Assess this cell for malaria.
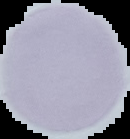
Uninfected.

Summary:
  - Image size: 130×139 pixels
  - Preparation: thin blood film
  - Image type: cell region segmented out of the field of view; surrounding area masked to black